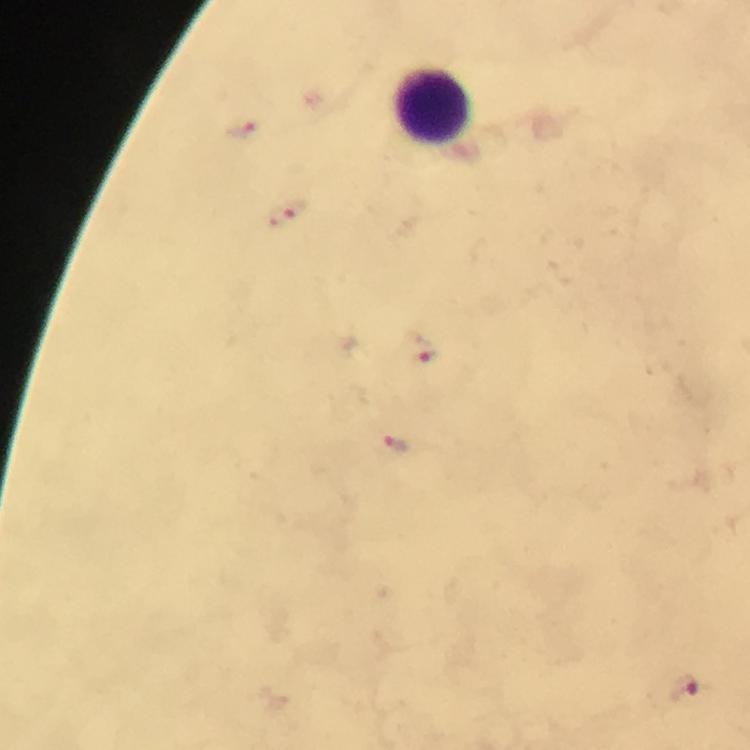

Approximate object centers, in pixels from the top-left corner. Leukocyte locations: (x=434, y=108). Plasmodium parasite locations: (x=243, y=130), (x=287, y=214), (x=418, y=347), (x=398, y=445), (x=685, y=690). 100x magnification. Cropped region of a single field of view. From a malaria diagnostic workup. Thick smear. Image is 750×750 pixels. Immersion oil was used. Giemsa-stained preparation. Photographed with a smartphone mounted on the microscope.